Identify the blood parasite species.
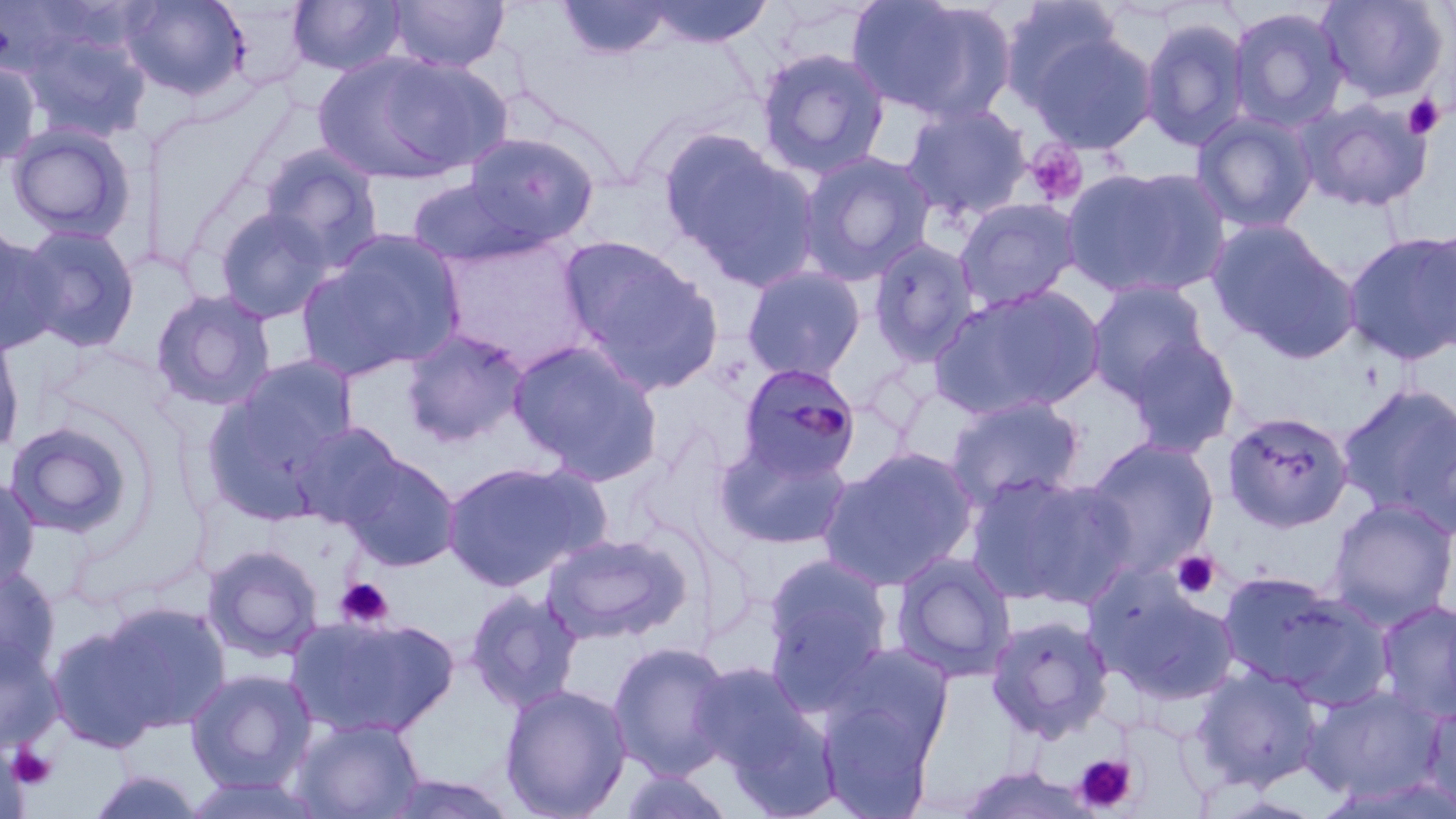

Plasmodium malariae.

Approximate bounding boxes as named x1/y1/x2/y2 corners in pixels. Platelet locations: (x1=1402, y1=94, x2=1444, y2=139), (x1=1024, y1=141, x2=1088, y2=208), (x1=1170, y1=550, x2=1221, y2=600), (x1=335, y1=577, x2=394, y2=629), (x1=8, y1=745, x2=58, y2=790), (x1=1072, y1=753, x2=1139, y2=814). Uninfected red blood cell locations: (x1=120, y1=0, x2=248, y2=100), (x1=288, y1=0, x2=407, y2=76), (x1=387, y1=0, x2=509, y2=72), (x1=556, y1=0, x2=676, y2=60), (x1=644, y1=0, x2=774, y2=48), (x1=847, y1=0, x2=1016, y2=125), (x1=1317, y1=0, x2=1448, y2=103), (x1=998, y1=1, x2=1128, y2=112), (x1=1227, y1=6, x2=1349, y2=133), (x1=1140, y1=16, x2=1251, y2=152), (x1=1023, y1=26, x2=1158, y2=155), (x1=20, y1=27, x2=152, y2=143), (x1=755, y1=47, x2=891, y2=179), (x1=316, y1=50, x2=508, y2=184), (x1=0, y1=57, x2=41, y2=172), (x1=1297, y1=96, x2=1434, y2=212), (x1=900, y1=102, x2=1033, y2=222), (x1=1191, y1=111, x2=1318, y2=234), (x1=6, y1=123, x2=137, y2=244), (x1=660, y1=131, x2=820, y2=288), (x1=459, y1=132, x2=599, y2=251), (x1=258, y1=144, x2=383, y2=268), (x1=797, y1=151, x2=935, y2=285), (x1=1060, y1=164, x2=1231, y2=301), (x1=406, y1=176, x2=539, y2=268), (x1=955, y1=198, x2=1081, y2=312), (x1=213, y1=205, x2=335, y2=324), (x1=1206, y1=219, x2=1359, y2=361), (x1=15, y1=223, x2=141, y2=352), (x1=0, y1=224, x2=61, y2=355), (x1=1417, y1=226, x2=1456, y2=356), (x1=299, y1=229, x2=467, y2=381), (x1=1342, y1=229, x2=1456, y2=365), (x1=560, y1=237, x2=723, y2=391), (x1=868, y1=238, x2=981, y2=365), (x1=741, y1=265, x2=866, y2=381), (x1=1085, y1=280, x2=1211, y2=403), (x1=929, y1=283, x2=1106, y2=420), (x1=150, y1=289, x2=277, y2=410), (x1=0, y1=327, x2=25, y2=457), (x1=401, y1=328, x2=528, y2=447), (x1=1124, y1=335, x2=1240, y2=456), (x1=508, y1=340, x2=663, y2=483), (x1=230, y1=354, x2=360, y2=467), (x1=201, y1=378, x2=353, y2=524), (x1=1337, y1=382, x2=1456, y2=530), (x1=944, y1=395, x2=1085, y2=511), (x1=1399, y1=400, x2=1455, y2=543), (x1=1222, y1=411, x2=1354, y2=533), (x1=3, y1=420, x2=140, y2=540), (x1=288, y1=420, x2=407, y2=529), (x1=713, y1=434, x2=854, y2=551), (x1=1082, y1=437, x2=1220, y2=577), (x1=820, y1=447, x2=978, y2=591), (x1=336, y1=451, x2=462, y2=572), (x1=440, y1=459, x2=606, y2=591), (x1=967, y1=471, x2=1134, y2=609), (x1=0, y1=477, x2=41, y2=596), (x1=1326, y1=498, x2=1456, y2=627), (x1=543, y1=532, x2=691, y2=643), (x1=202, y1=544, x2=325, y2=663), (x1=762, y1=551, x2=895, y2=696), (x1=892, y1=551, x2=1017, y2=682), (x1=0, y1=567, x2=62, y2=684), (x1=1216, y1=570, x2=1372, y2=701), (x1=1089, y1=573, x2=1240, y2=707), (x1=464, y1=587, x2=583, y2=713), (x1=1376, y1=598, x2=1456, y2=723), (x1=94, y1=600, x2=231, y2=733), (x1=984, y1=614, x2=1114, y2=744), (x1=288, y1=615, x2=459, y2=738), (x1=47, y1=622, x2=168, y2=753), (x1=0, y1=636, x2=62, y2=755), (x1=607, y1=640, x2=736, y2=780), (x1=826, y1=643, x2=955, y2=760), (x1=689, y1=660, x2=822, y2=783), (x1=1190, y1=665, x2=1324, y2=792), (x1=184, y1=668, x2=318, y2=792), (x1=499, y1=683, x2=632, y2=819), (x1=1301, y1=684, x2=1445, y2=802), (x1=817, y1=696, x2=937, y2=819), (x1=1420, y1=703, x2=1456, y2=814), (x1=292, y1=717, x2=426, y2=818), (x1=0, y1=745, x2=31, y2=819), (x1=615, y1=766, x2=738, y2=819), (x1=85, y1=769, x2=208, y2=818), (x1=377, y1=771, x2=522, y2=818), (x1=179, y1=774, x2=328, y2=818), (x1=1317, y1=775, x2=1456, y2=819). Plasmodium malariae-infected red blood cell locations: (x1=737, y1=364, x2=861, y2=482). 1000x magnification. Thin blood smear. Optical microscopy. May-Grünwald-Giemsa-stained preparation. Image is 1456×819 pixels. One field of a larger specimen.